Identify the parasite.
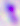
Toxoplasma gondii.

Summary:
  - Magnification: 400x
  - Modality: photomicrograph